Identify the parasite.
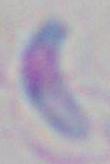
This is Toxoplasma gondii.

Captured at 1000x magnification. Micrograph.